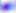

Toxoplasma gondii is shown. Captured at 400x magnification. Photomicrograph.